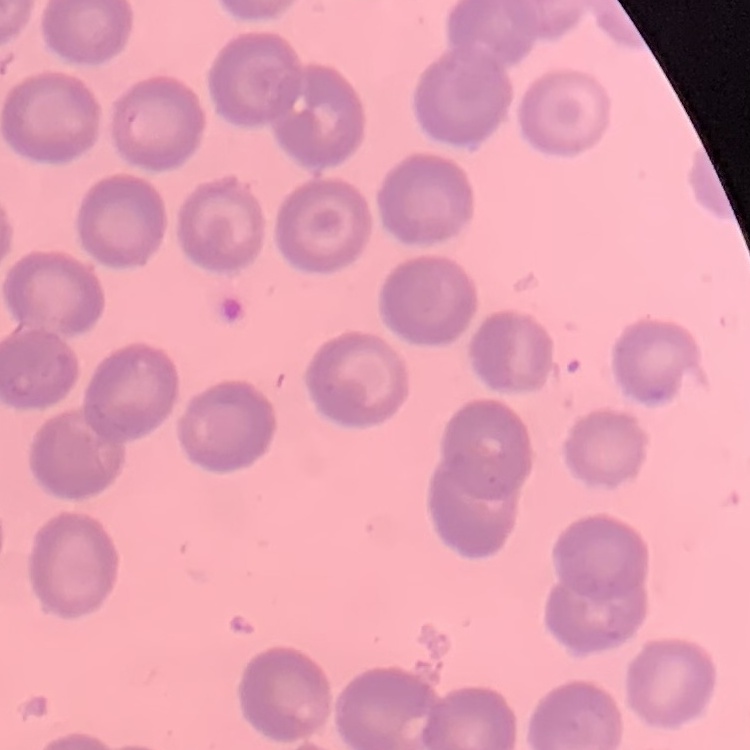

Summary:
  - Red blood cell morphology: no rouleaux formation
  - Stain: Field's or Giemsa
  - Image type: one tile cut from a larger photomicrograph
  - Preparation: thin peripheral smear